Assess this cell for malaria.
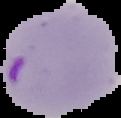

It is parasitized.

Summary:
  - Image size: 121×118 pixels
  - Preparation: thin blood film
  - Image type: cell region segmented out of the field of view; surrounding area masked to black